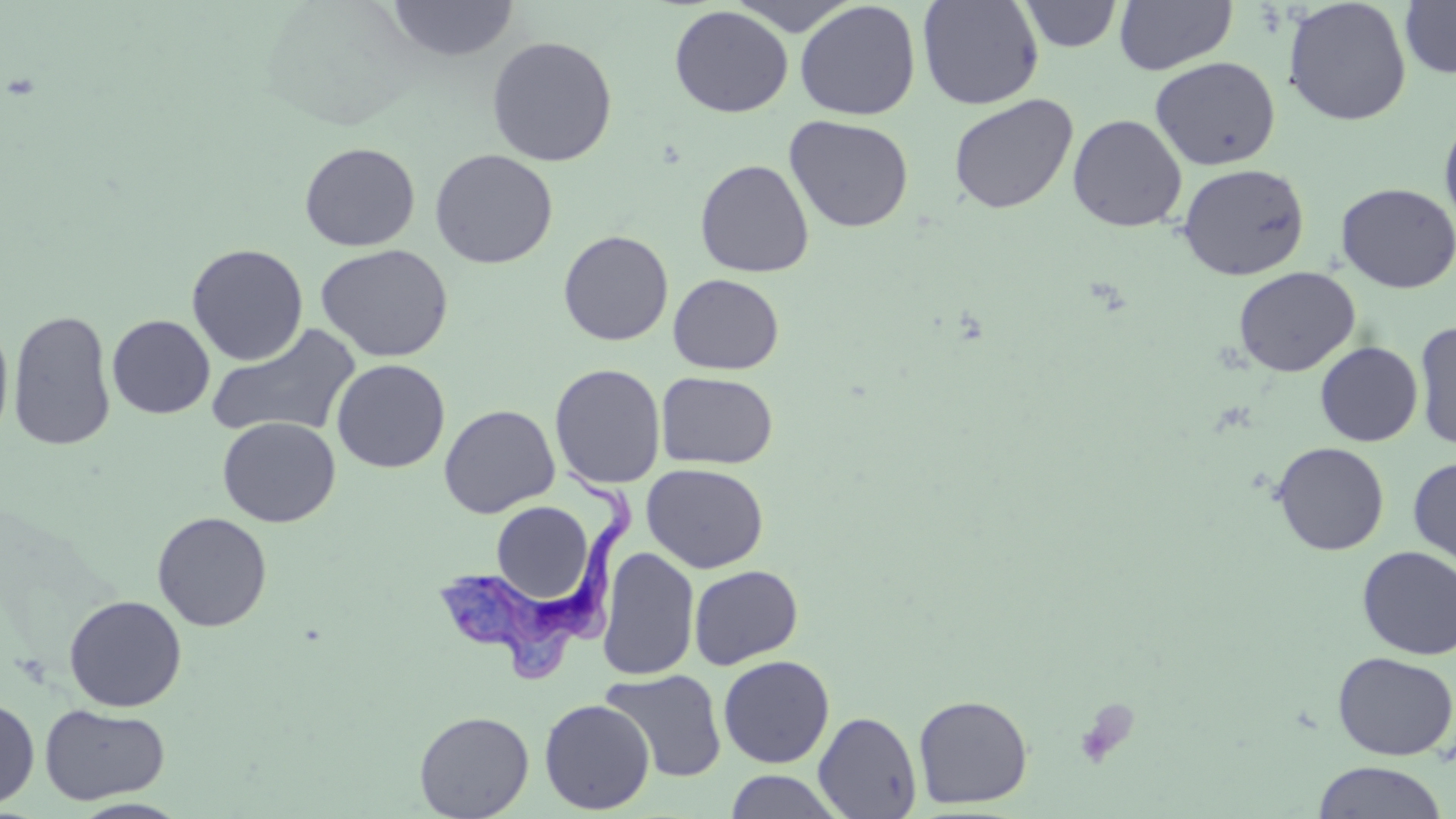
slide-level diagnosis = Trypanosoma brucei
modality = optical microscopy
magnification = 1000x
preparation = thin blood smear
field of view = single
platelet locations = approximate bounding boxes as (x1, y1, x2, y2) in pixels: (1074, 698, 1138, 768)
stain = May-Grünwald-Giemsa
Trypanosoma brucei locations = approximate bounding boxes as (x1, y1, x2, y2) in pixels: (435, 469, 639, 686)
uninfected red blood cell locations = approximate bounding boxes as (x1, y1, x2, y2) in pixels: (725, 0, 862, 35), (917, 0, 1043, 110), (1113, 0, 1237, 75), (1282, 0, 1412, 127), (1400, 0, 1456, 79), (386, 1, 519, 61), (794, 1, 921, 120), (1018, 1, 1123, 52), (669, 5, 793, 117), (486, 35, 618, 167), (1150, 56, 1281, 170), (948, 93, 1078, 215), (1439, 111, 1456, 235), (1067, 113, 1187, 232), (784, 115, 914, 233), (299, 142, 420, 251), (429, 149, 558, 269), (695, 159, 814, 278), (1177, 162, 1309, 280), (1335, 182, 1456, 293), (558, 230, 674, 346), (186, 243, 308, 366), (315, 244, 453, 362), (1233, 266, 1360, 376), (668, 273, 784, 375), (7, 309, 117, 451), (107, 314, 214, 419), (0, 317, 14, 446), (1413, 320, 1456, 452), (205, 324, 362, 441), (1315, 341, 1423, 446), (331, 359, 450, 473), (549, 363, 666, 489), (655, 371, 778, 469), (438, 404, 560, 518), (217, 417, 341, 527), (1271, 441, 1389, 555), (1408, 456, 1456, 573), (642, 463, 769, 573), (491, 501, 594, 605), (152, 512, 272, 631), (1357, 545, 1456, 660), (597, 546, 700, 681), (688, 564, 803, 669), (63, 594, 187, 712), (1332, 651, 1456, 760), (718, 655, 835, 768), (600, 668, 727, 783), (913, 694, 1033, 809), (0, 696, 39, 810), (539, 698, 655, 814), (40, 703, 170, 805), (414, 710, 534, 819), (813, 711, 922, 818), (1312, 761, 1448, 819), (724, 770, 846, 818)
image size = 1456×819 pixels